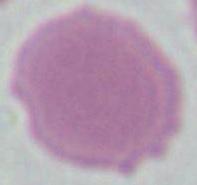 A red blood cell is seen. Captured at 1000x magnification. Micrograph.